Classify this cell by malaria status.
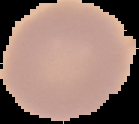
It is uninfected.

image_size: 139×124 pixels
preparation: thin blood film
image_type: segmented cell region on a black background